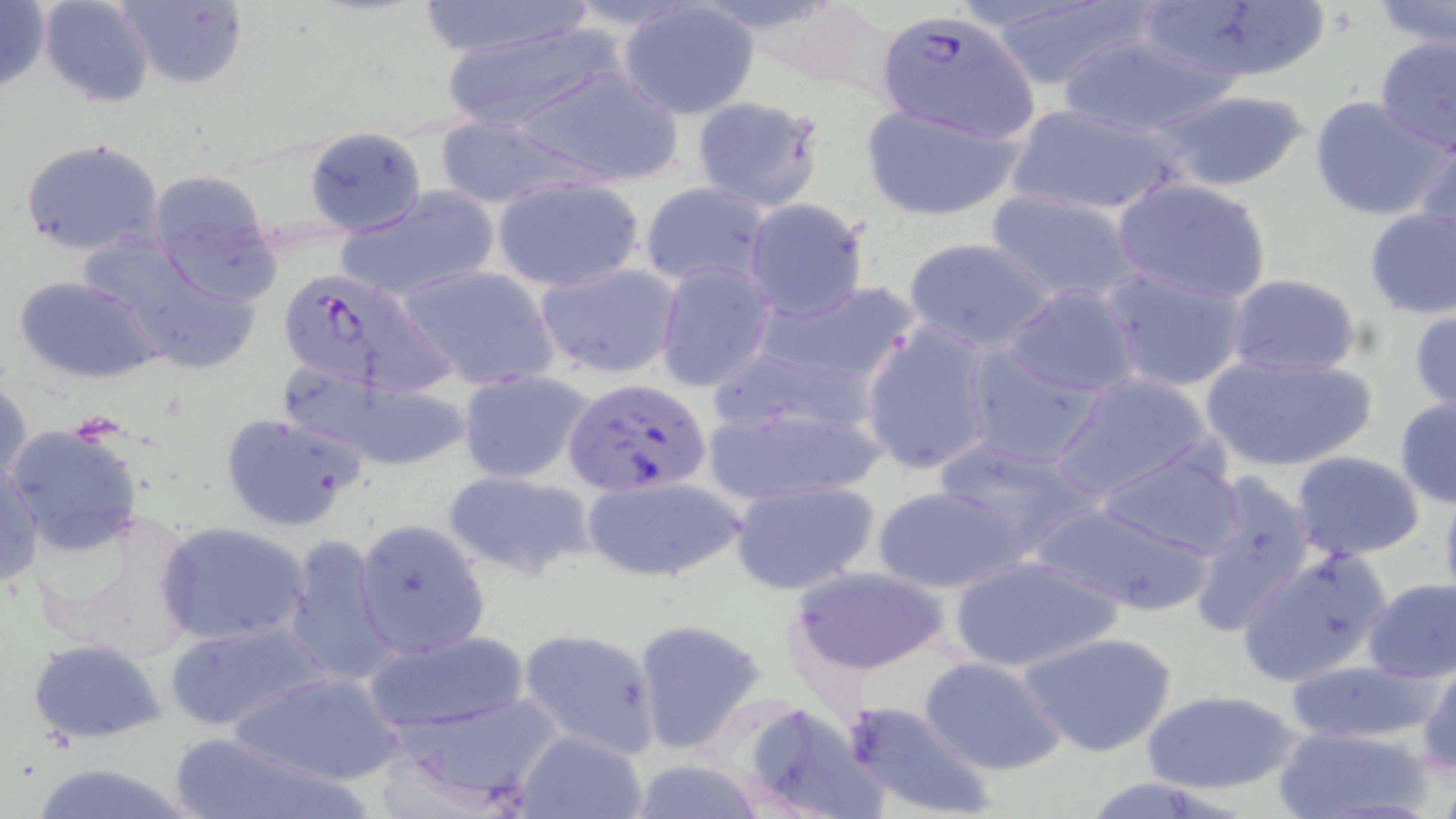 Approximate bounding boxes as [x1, y1, x2, y2] in pixels. Plasmodium falciparum-infected red blood cell locations: [881, 15, 1047, 139], [276, 267, 448, 395], [561, 377, 713, 498]. Uninfected red blood cell locations: [0, 0, 51, 96], [37, 0, 156, 107], [115, 0, 248, 90], [413, 0, 597, 60], [979, 0, 1158, 94], [1133, 0, 1329, 87], [1374, 0, 1456, 48], [616, 3, 760, 120], [740, 4, 901, 98], [442, 24, 626, 134], [1055, 31, 1239, 139], [1373, 36, 1456, 151], [509, 66, 686, 188], [1146, 87, 1315, 194], [689, 93, 827, 212], [1308, 94, 1449, 221], [859, 102, 1025, 221], [1003, 103, 1190, 218], [432, 116, 588, 209], [303, 126, 426, 237], [1412, 130, 1456, 248], [18, 136, 164, 259], [145, 169, 282, 297], [493, 176, 645, 292], [1112, 177, 1273, 305], [639, 182, 772, 289], [336, 187, 500, 303], [985, 190, 1144, 304], [742, 198, 871, 322], [1361, 206, 1456, 319], [76, 231, 263, 376], [901, 235, 1059, 352], [534, 262, 680, 382], [652, 262, 776, 393], [396, 263, 559, 391], [1100, 266, 1250, 393], [1225, 274, 1364, 378], [14, 275, 162, 384], [1002, 282, 1142, 399], [754, 283, 918, 402], [1409, 304, 1456, 417], [860, 321, 994, 476], [962, 345, 1104, 470], [1200, 349, 1380, 474], [280, 366, 468, 470], [458, 371, 596, 485], [1051, 371, 1217, 502], [0, 374, 33, 497], [700, 389, 891, 506], [1394, 395, 1456, 509], [219, 410, 368, 531], [3, 422, 146, 558], [931, 437, 1102, 561], [1095, 448, 1248, 560], [1291, 452, 1425, 561], [1, 459, 44, 590], [442, 469, 595, 579], [1183, 470, 1319, 640], [577, 474, 744, 586], [728, 477, 881, 596], [1438, 478, 1456, 612], [872, 483, 1030, 595], [1028, 499, 1214, 616], [26, 503, 206, 670], [353, 518, 490, 660], [157, 521, 311, 647], [281, 533, 398, 690], [1234, 546, 1392, 687], [949, 555, 1123, 674], [785, 563, 952, 677], [1359, 577, 1456, 682], [161, 618, 332, 734], [630, 618, 769, 754], [517, 628, 664, 758], [361, 630, 534, 734], [1020, 630, 1179, 758], [27, 639, 166, 743], [916, 654, 1066, 777], [1283, 659, 1439, 745], [1416, 659, 1456, 775], [224, 669, 408, 785], [1141, 689, 1302, 796], [376, 690, 565, 815], [842, 699, 999, 819], [734, 700, 894, 819], [1271, 724, 1433, 818], [516, 729, 650, 819], [167, 733, 378, 819], [622, 758, 773, 818], [24, 763, 204, 819]. Slide-level diagnosis: Plasmodium falciparum. Captured at 1000x magnification. Thin blood film. One field of a larger specimen. Light microscopy. May-Grünwald-Giemsa-stained preparation. Image is 1456×819 pixels.